Classify this cell by malaria status.
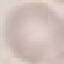

It is uninfected.

stain = Giemsa
capture = smartphone camera at the microscope eyepiece
preparation = thin blood film
image type = automatically extracted cell patch, resized to 64 × 64 pixels